Name the parasite shown.
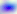
Toxoplasma gondii.

Summary:
  - Modality: photomicrograph
  - Magnification: 400x